Name the parasite shown.
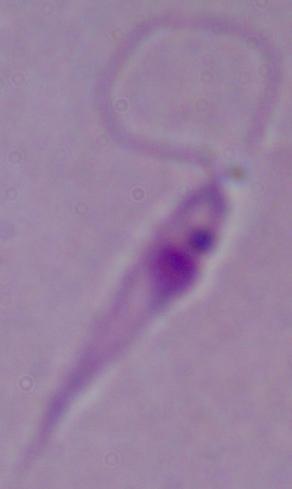
Leishmania.

Summary:
  - Modality: micrograph
  - Magnification: 1000x